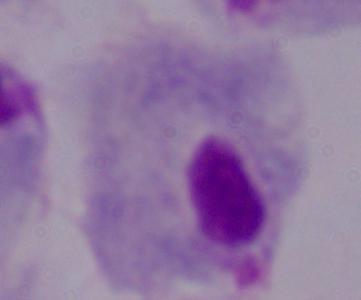

A trichomonad is shown. Micrograph. Captured at 1000x magnification.